Comment on the morphology of the red blood cells.
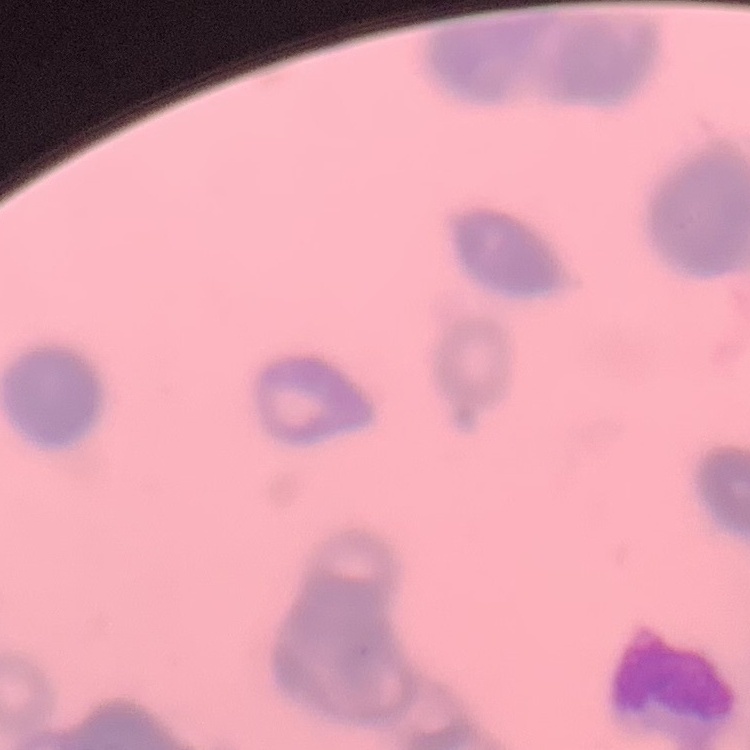
They show rouleaux formation.

Square crop of a larger photomicrograph. Thin peripheral smear. Field's or Giemsa stain.